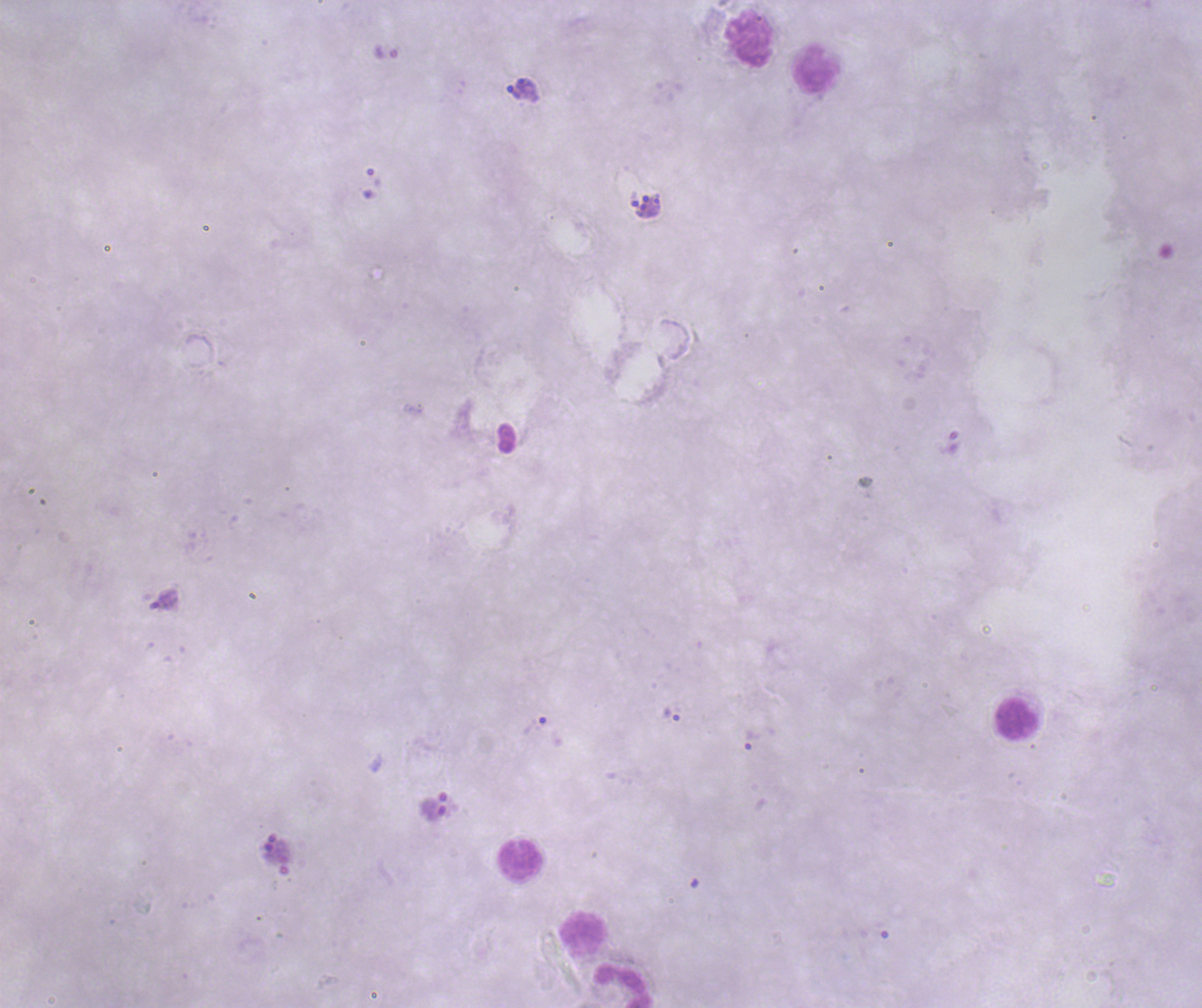
{
  "life_cycle_stages_observed": "trophozoite, schizont",
  "context": "previously used in a real diagnosis",
  "image_size": "1202×1008 pixels",
  "stain": "Romanowsky",
  "leukocyte_locations": "approximate centers as (x, y) in pixels: (749, 39), (817, 69), (1017, 719), (522, 862), (583, 932), (624, 984)",
  "trophozoite_locations": "approximate centers as (x, y) in pixels: (523, 84), (513, 92), (671, 714), (536, 725), (752, 740)",
  "schizont_locations": "approximate centers as (x, y) in pixels: (645, 207)",
  "background_quality": "unsatisfactory",
  "magnification": "100x",
  "preparation": "thick blood smear",
  "field_of_view": "one from this slide",
  "coloration_quality": "bad",
  "result": "Plasmodium parasites identified"
}